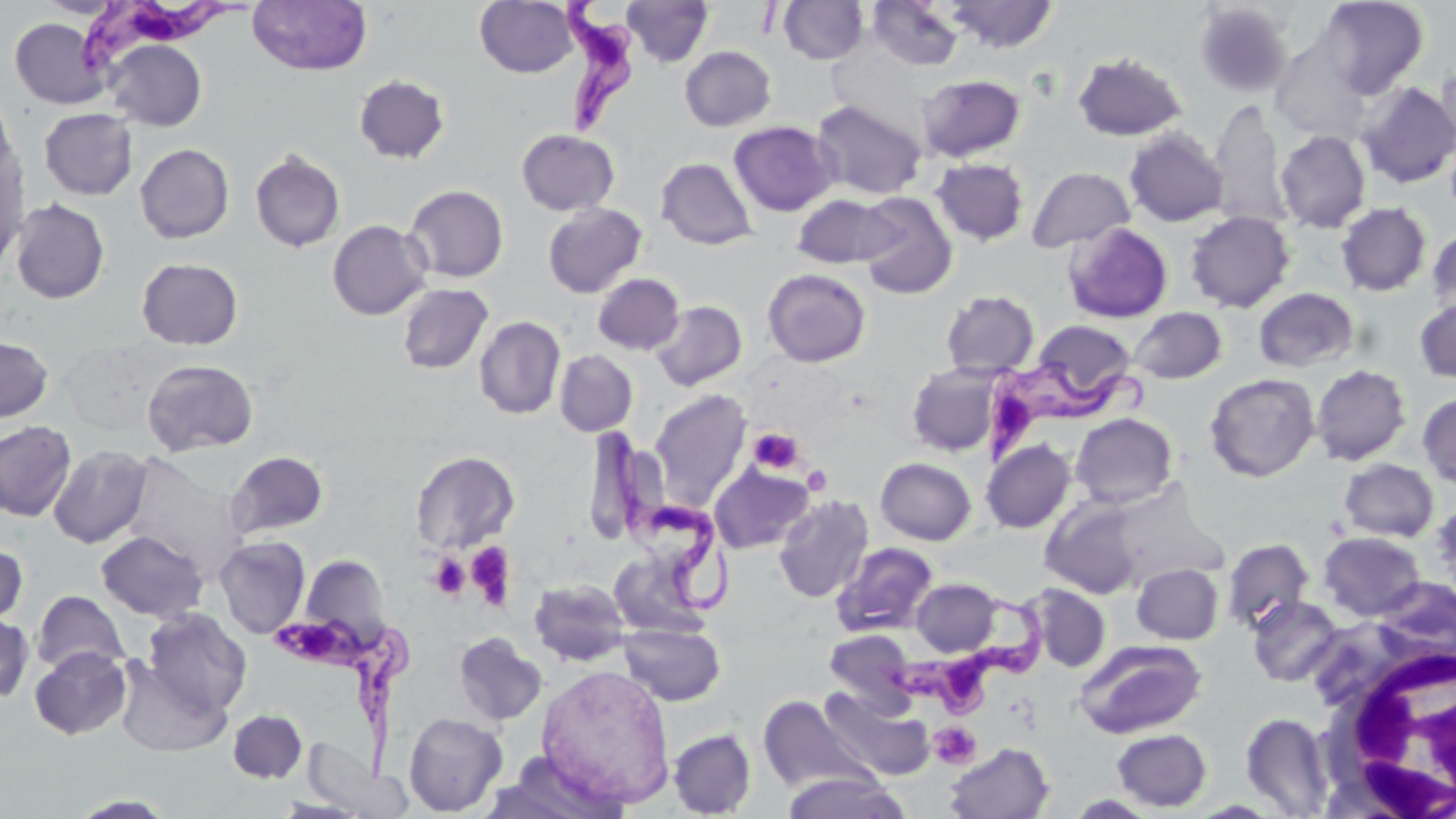
Summary:
  - Coordinate format: approximate bounding boxes as named x1/y1/x2/y2 corners in pixels
  - Platelet locations: (x1=747, y1=427, x2=804, y2=474), (x1=801, y1=465, x2=831, y2=494), (x1=465, y1=542, x2=517, y2=609), (x1=430, y1=554, x2=470, y2=599), (x1=929, y1=722, x2=981, y2=769)
  - White blood cell locations: (x1=1318, y1=643, x2=1456, y2=817)
  - Trypanosoma brucei locations: (x1=71, y1=0, x2=255, y2=78), (x1=556, y1=0, x2=634, y2=136), (x1=983, y1=362, x2=1154, y2=470), (x1=607, y1=427, x2=736, y2=616), (x1=878, y1=596, x2=1050, y2=722), (x1=272, y1=619, x2=416, y2=782)
  - Uninfected red blood cell locations: (x1=474, y1=0, x2=580, y2=78), (x1=621, y1=0, x2=715, y2=67), (x1=942, y1=0, x2=1060, y2=53), (x1=1316, y1=0, x2=1429, y2=99), (x1=247, y1=1, x2=372, y2=76), (x1=778, y1=1, x2=869, y2=65), (x1=867, y1=1, x2=965, y2=71), (x1=1194, y1=3, x2=1294, y2=99), (x1=9, y1=17, x2=111, y2=109), (x1=104, y1=39, x2=207, y2=131), (x1=680, y1=46, x2=776, y2=131), (x1=1072, y1=51, x2=1188, y2=141), (x1=1435, y1=61, x2=1456, y2=158), (x1=353, y1=74, x2=450, y2=164), (x1=917, y1=74, x2=1026, y2=163), (x1=1355, y1=81, x2=1456, y2=188), (x1=0, y1=84, x2=18, y2=183), (x1=810, y1=99, x2=926, y2=200), (x1=1208, y1=99, x2=1290, y2=231), (x1=39, y1=108, x2=137, y2=200), (x1=729, y1=121, x2=838, y2=216), (x1=516, y1=128, x2=619, y2=215), (x1=1124, y1=128, x2=1228, y2=227), (x1=1274, y1=130, x2=1371, y2=233), (x1=135, y1=143, x2=235, y2=243), (x1=250, y1=150, x2=345, y2=253), (x1=0, y1=154, x2=28, y2=275), (x1=656, y1=157, x2=757, y2=250), (x1=930, y1=158, x2=1029, y2=246), (x1=1026, y1=166, x2=1135, y2=253), (x1=404, y1=184, x2=508, y2=283), (x1=855, y1=192, x2=958, y2=300), (x1=792, y1=193, x2=901, y2=269), (x1=10, y1=198, x2=110, y2=304), (x1=1336, y1=202, x2=1431, y2=297), (x1=543, y1=203, x2=646, y2=298), (x1=1185, y1=211, x2=1295, y2=313), (x1=327, y1=219, x2=431, y2=320), (x1=1063, y1=222, x2=1173, y2=323), (x1=1426, y1=227, x2=1456, y2=317), (x1=137, y1=257, x2=243, y2=350), (x1=762, y1=268, x2=871, y2=367), (x1=593, y1=273, x2=684, y2=355), (x1=397, y1=283, x2=494, y2=374), (x1=1253, y1=287, x2=1359, y2=373), (x1=941, y1=290, x2=1039, y2=377), (x1=1414, y1=297, x2=1456, y2=383), (x1=651, y1=300, x2=747, y2=391), (x1=1128, y1=307, x2=1227, y2=384), (x1=474, y1=316, x2=566, y2=419), (x1=1032, y1=320, x2=1137, y2=404), (x1=0, y1=335, x2=54, y2=422), (x1=554, y1=350, x2=637, y2=436), (x1=141, y1=358, x2=258, y2=457), (x1=906, y1=363, x2=1003, y2=456), (x1=1310, y1=364, x2=1411, y2=466), (x1=1205, y1=373, x2=1320, y2=482), (x1=649, y1=389, x2=751, y2=511), (x1=1417, y1=392, x2=1456, y2=490), (x1=1070, y1=413, x2=1178, y2=509), (x1=0, y1=420, x2=76, y2=522), (x1=981, y1=439, x2=1075, y2=533), (x1=47, y1=445, x2=152, y2=548), (x1=226, y1=450, x2=329, y2=539), (x1=410, y1=450, x2=520, y2=554), (x1=121, y1=453, x2=246, y2=575), (x1=875, y1=457, x2=976, y2=545), (x1=1339, y1=458, x2=1438, y2=542), (x1=709, y1=463, x2=813, y2=554), (x1=774, y1=494, x2=874, y2=603), (x1=1040, y1=495, x2=1145, y2=599), (x1=1431, y1=499, x2=1456, y2=594), (x1=96, y1=531, x2=209, y2=622), (x1=1318, y1=532, x2=1425, y2=621), (x1=214, y1=536, x2=311, y2=638), (x1=1220, y1=537, x2=1314, y2=634), (x1=0, y1=541, x2=28, y2=630), (x1=831, y1=542, x2=938, y2=637), (x1=300, y1=553, x2=390, y2=645), (x1=1131, y1=563, x2=1223, y2=644), (x1=529, y1=578, x2=631, y2=667), (x1=911, y1=578, x2=1002, y2=657), (x1=1024, y1=584, x2=1110, y2=672), (x1=33, y1=590, x2=129, y2=677), (x1=1247, y1=596, x2=1344, y2=687), (x1=142, y1=607, x2=252, y2=715), (x1=0, y1=615, x2=33, y2=703), (x1=618, y1=621, x2=725, y2=706), (x1=823, y1=630, x2=917, y2=714), (x1=453, y1=632, x2=548, y2=726), (x1=1076, y1=638, x2=1208, y2=738), (x1=30, y1=646, x2=131, y2=740), (x1=114, y1=658, x2=230, y2=757), (x1=536, y1=664, x2=675, y2=808), (x1=820, y1=686, x2=934, y2=781), (x1=757, y1=693, x2=875, y2=794), (x1=228, y1=710, x2=307, y2=784), (x1=403, y1=712, x2=507, y2=816), (x1=1240, y1=712, x2=1335, y2=816), (x1=1111, y1=728, x2=1212, y2=812), (x1=668, y1=729, x2=756, y2=817), (x1=944, y1=742, x2=1055, y2=819), (x1=305, y1=745, x2=402, y2=817), (x1=483, y1=754, x2=627, y2=819), (x1=780, y1=770, x2=910, y2=818), (x1=69, y1=794, x2=176, y2=818), (x1=1065, y1=794, x2=1160, y2=818)
  - Slide-level diagnosis: Trypanosoma brucei
  - Field of view: single
  - Magnification: 1000x
  - Image size: 1456×819 pixels
  - Preparation: thin blood film
  - Stain: May-Grünwald-Giemsa
  - Modality: optical microscopy